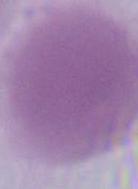
{
  "modality": "photomicrograph",
  "identification": "red blood cell",
  "magnification": "1000x"
}